State the preparation type.
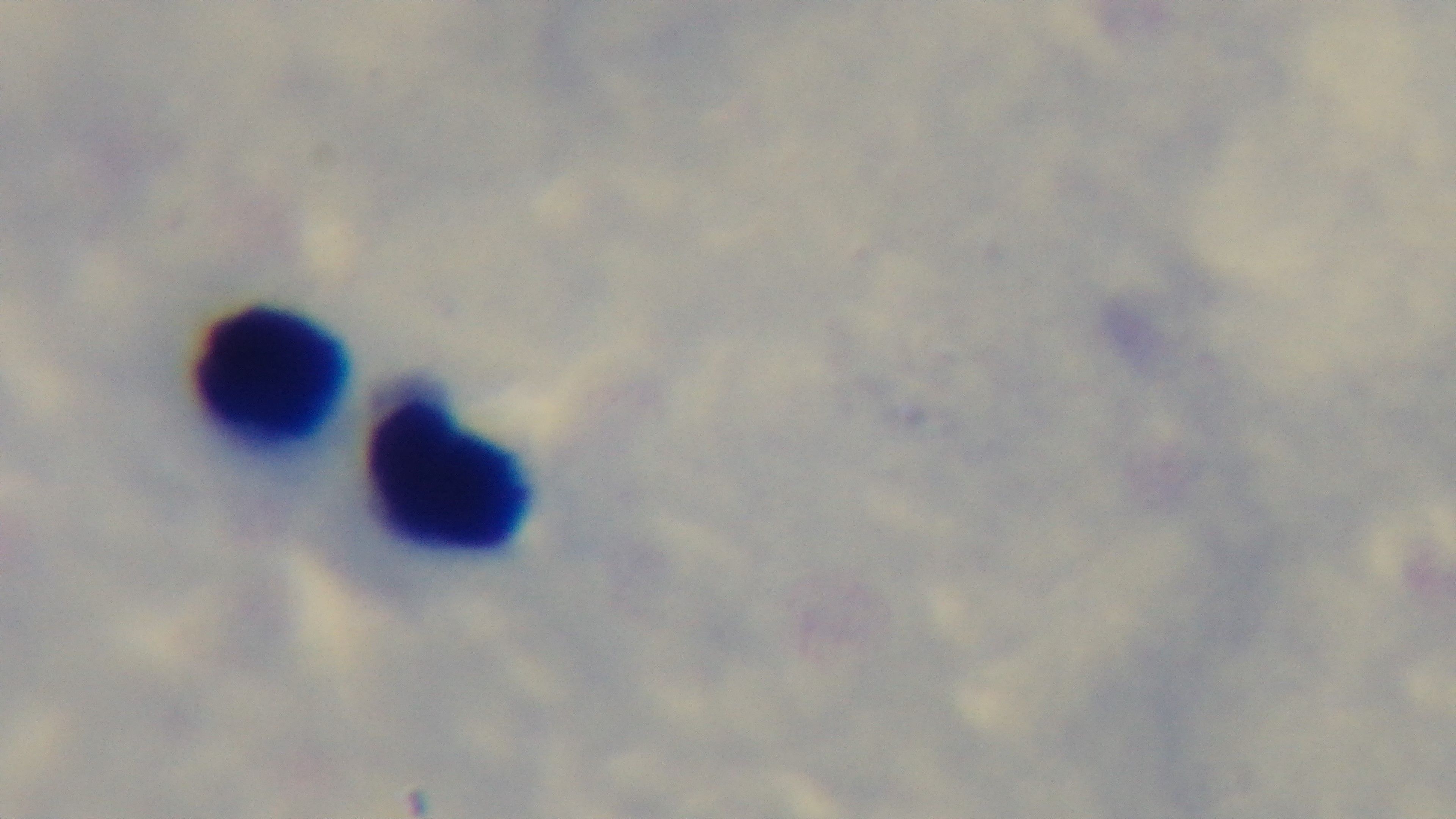
It is a thick blood film.

Summary:
  - Stain: Giemsa
  - Modality: light microscopy
  - Objective: 100x oil immersion
  - Malaria status: uninfected
  - Field of view: one from the slide
  - Capture: mounted 4K digital camera